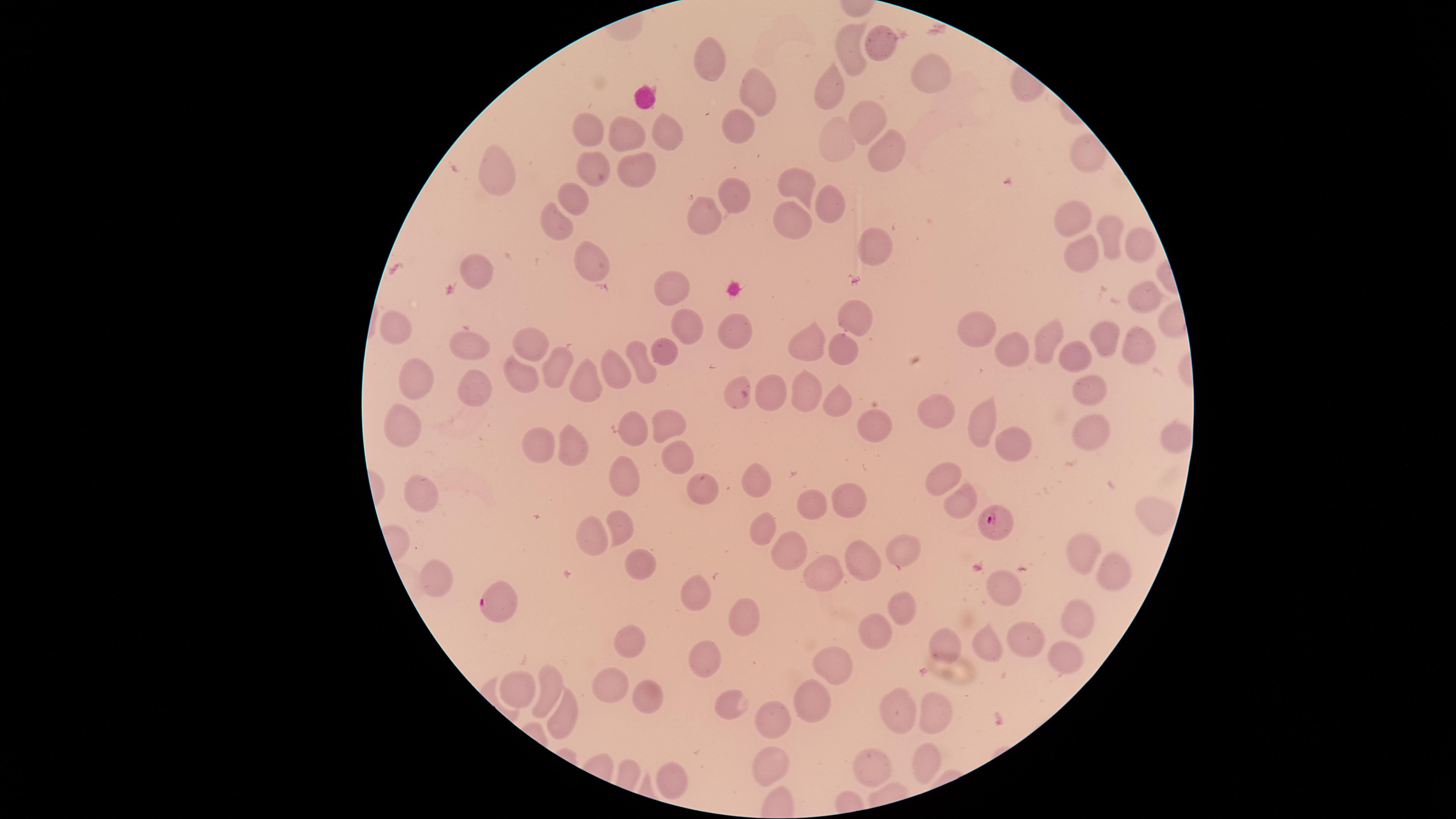
Approximate marker points as [x, y] in pixels. Uninfected RBCs: [845, 43], [878, 47], [710, 56], [924, 71], [833, 89], [756, 100], [863, 120], [663, 129], [588, 131], [621, 131], [742, 131], [837, 145], [883, 146], [1083, 154], [637, 170], [600, 171], [495, 174], [800, 182], [730, 195], [574, 199], [832, 207], [1071, 220], [796, 224], [706, 227], [556, 228], [1108, 231], [1136, 236], [879, 239], [1090, 260], [481, 267], [602, 268], [666, 292], [1144, 297], [863, 319], [685, 332], [732, 332], [404, 334], [979, 334], [1142, 341], [1105, 342], [469, 346], [804, 347], [1050, 348], [530, 349], [667, 351], [843, 351], [1006, 356], [1077, 361], [636, 368], [556, 371], [611, 375], [423, 377], [1083, 383], [518, 384], [583, 384], [472, 388], [768, 388], [801, 390], [739, 391], [842, 404], [937, 412], [978, 424], [669, 426], [1091, 426], [875, 427], [403, 429], [638, 435], [538, 442], [571, 442], [1017, 443], [677, 460], [625, 479], [947, 480], [754, 486], [698, 491], [428, 495], [810, 495], [849, 504], [960, 509], [1147, 512], [618, 522], [598, 529], [762, 533], [1077, 550], [792, 551], [901, 556], [635, 559], [867, 563], [1119, 574], [438, 577], [822, 580], [1002, 587], [696, 592], [905, 608], [1079, 614], [744, 617], [876, 635], [1027, 640], [992, 644], [631, 645], [947, 646], [1067, 659], [701, 664], [830, 668], [611, 682], [517, 685], [521, 689], [551, 694], [645, 696], [813, 699], [731, 704], [893, 707], [935, 716], [777, 720], [561, 722], [772, 756], [874, 760], [924, 760], [667, 773]. Parasitized RBCs: [997, 526], [498, 602]. Image is 1456×819 pixels. Thin blood film. Presence: malaria parasites identified. Giemsa-stained preparation. The visible region is circular. Smartphone photograph through the microscope eyepiece. Species: Plasmodium falciparum. One field of view of the specimen.